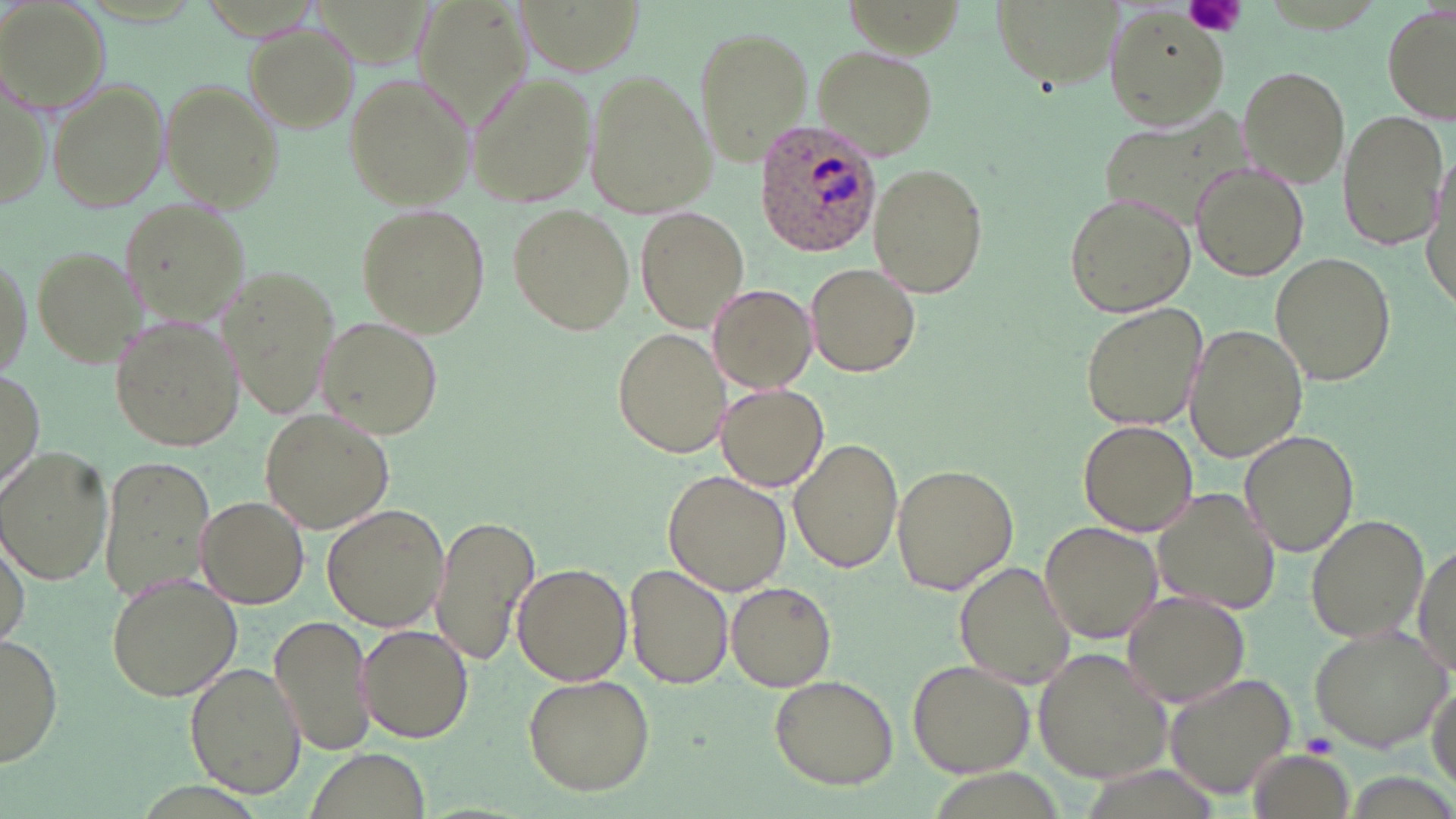
Summary:
  - Coordinate format: approximate bounding boxes as (x1,y1)-(x2,y2) corner pairs in pixels
  - Plasmodium ovale-infected red blood cell locations: (755,119)-(886,256)
  - Uninfected red blood cell locations: (409,4)-(535,139), (0,5)-(107,114), (1382,5)-(1455,127), (986,8)-(1133,99), (1103,11)-(1231,133), (244,21)-(360,133), (693,26)-(812,164), (812,45)-(939,161), (1236,64)-(1351,185), (582,68)-(717,221), (468,72)-(595,207), (344,74)-(476,210), (0,75)-(50,209), (46,79)-(168,212), (161,79)-(285,214), (1099,103)-(1268,230), (1338,111)-(1448,250), (1190,161)-(1308,283), (870,165)-(986,295), (1064,192)-(1195,318), (118,196)-(251,333), (356,205)-(489,336), (508,205)-(634,336), (637,207)-(750,332), (0,247)-(31,379), (34,247)-(145,365), (1270,253)-(1396,387), (805,261)-(922,377), (222,265)-(343,421), (708,283)-(817,391), (1079,301)-(1208,431), (315,317)-(445,439), (111,319)-(239,451), (1186,323)-(1309,464), (611,328)-(729,461), (0,370)-(43,496), (717,384)-(828,492), (260,409)-(394,534), (1077,418)-(1200,535), (1239,430)-(1359,555), (790,438)-(904,573), (0,448)-(112,587), (100,455)-(216,603), (891,466)-(1017,594), (663,470)-(792,595), (1152,488)-(1282,614), (195,496)-(310,609), (321,504)-(448,631), (432,513)-(539,669), (1305,514)-(1428,645), (1039,520)-(1162,645), (1,528)-(30,650), (1412,540)-(1456,674), (513,560)-(632,686), (954,560)-(1077,688), (624,563)-(734,690), (106,573)-(241,700), (727,580)-(837,691), (1121,591)-(1252,709), (268,613)-(376,758), (359,624)-(474,744), (1309,624)-(1451,753), (0,634)-(63,768), (1033,649)-(1175,783), (907,660)-(1037,780), (186,662)-(306,799), (1163,672)-(1299,800), (521,673)-(656,795), (769,674)-(898,789), (1427,678)-(1455,792), (303,749)-(432,819), (1245,751)-(1353,819)
  - Platelet locations: (1185,0)-(1245,38), (1303,732)-(1341,758)
  - Slide-level diagnosis: Plasmodium ovale
  - Preparation: thin blood film
  - Image size: 1456×819 pixels
  - Magnification: 1000x
  - Stain: May-Grünwald-Giemsa
  - Modality: light microscopy
  - Field of view: one of a larger specimen